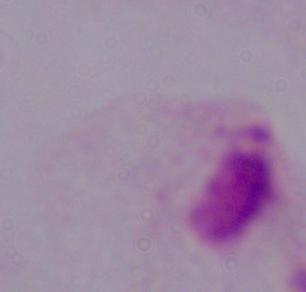
Micrograph. A trichomonad is seen. 1000x magnification.